Assess this cell for malaria.
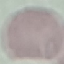
Uninfected.

image type = automatically extracted cell patch, resized to 64 × 64 pixels
capture = smartphone camera at the microscope eyepiece
preparation = thin blood film
stain = Giemsa